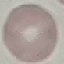 Result: no malaria parasites detected. Thin blood film. Automatically extracted cell patch, resized to 64 × 64 pixels. Photographed with a smartphone camera at the microscope eyepiece. Giemsa-stained preparation.